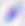

modality = photomicrograph
identification = Toxoplasma gondii
magnification = 400x